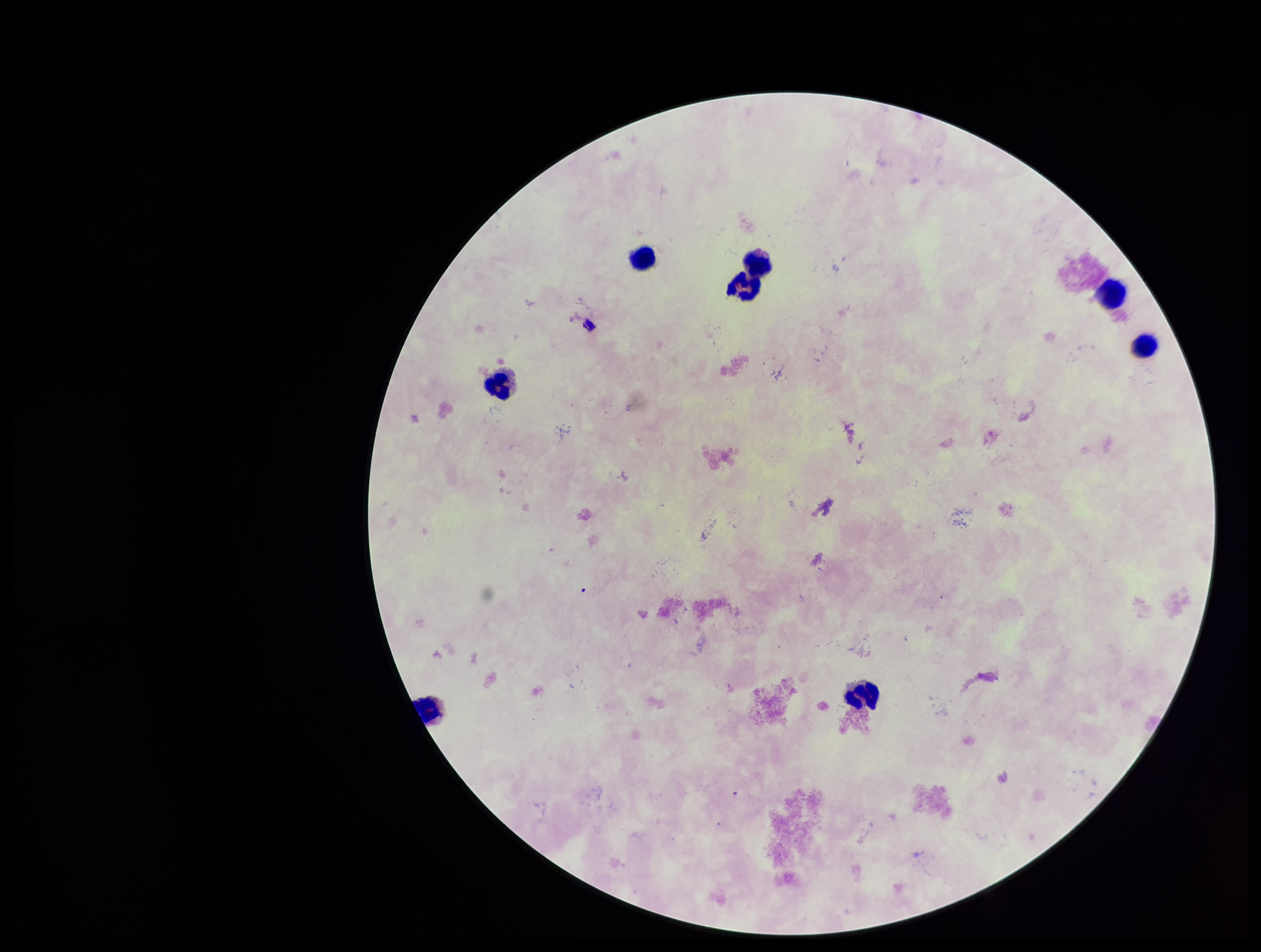

Preparation: thick blood smear. Parasite count: 0. One field from this slide. Smartphone photograph taken through the eyepiece of a microscope. Stained with Giemsa. Image is 1261×952 pixels. Leukocyte count: 8. Plasmodium parasites: none identified. Patient malaria status: negative.